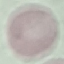

Malaria status: uninfected. Automatically extracted cell patch, resized to 64 × 64 pixels. Photographed with a smartphone camera at the microscope eyepiece. Giemsa stain. Thin blood smear.